Outline each blood parasite and name the species.
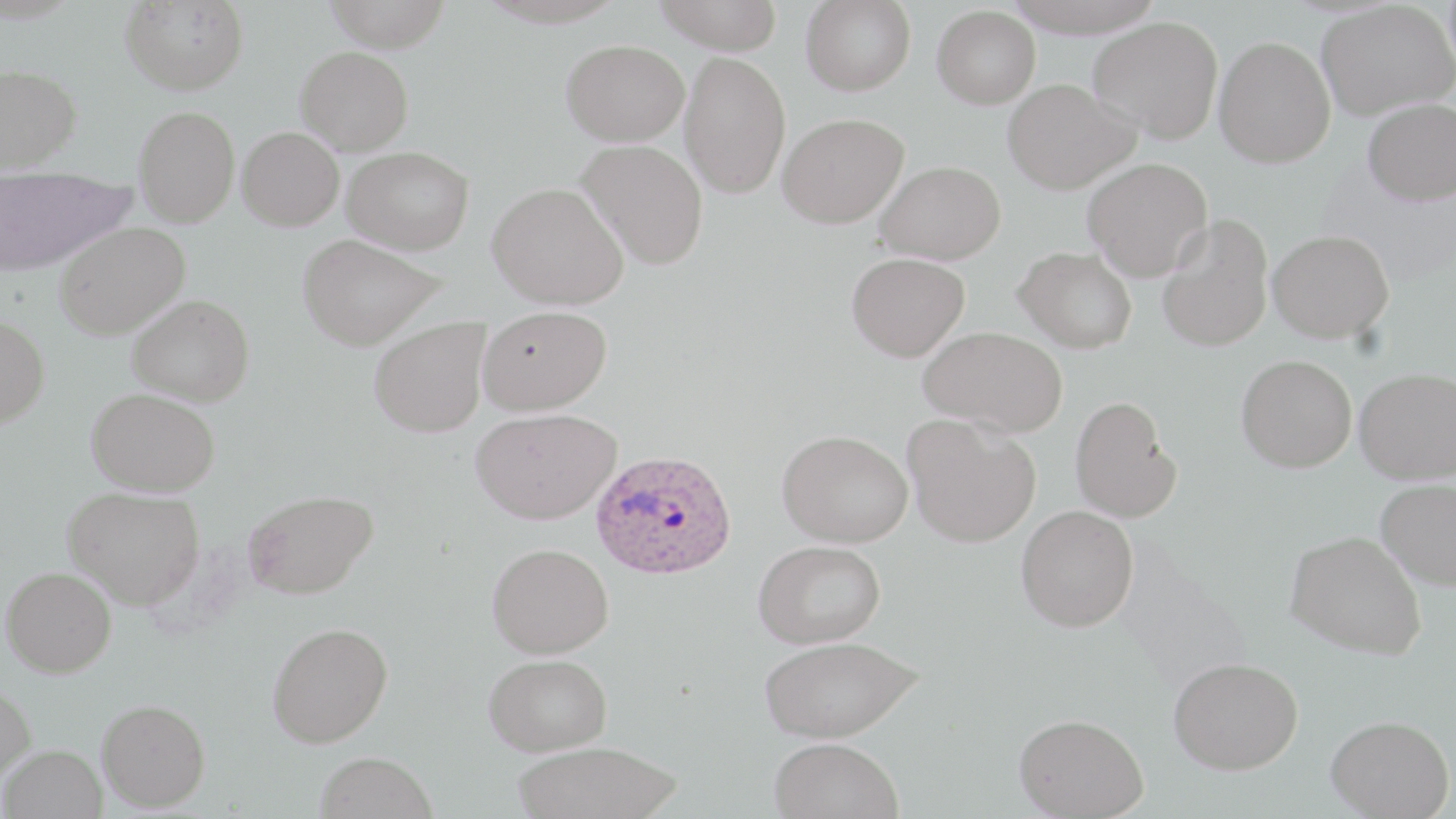

Approximate bounding boxes as named x1/y1/x2/y2 corners in pixels.
Plasmodium ovale-infected red blood cells: (x1=590, y1=448, x2=737, y2=580).
No Plasmodium falciparum, Plasmodium malariae, Plasmodium vivax, Babesia divergens, or Trypanosoma brucei observed.

Uninfected red blood cell locations: (x1=322, y1=0, x2=452, y2=52), (x1=653, y1=0, x2=785, y2=54), (x1=801, y1=0, x2=916, y2=96), (x1=119, y1=1, x2=249, y2=95), (x1=1316, y1=1, x2=1455, y2=120), (x1=932, y1=5, x2=1040, y2=108), (x1=1088, y1=16, x2=1224, y2=143), (x1=1214, y1=36, x2=1336, y2=168), (x1=561, y1=39, x2=690, y2=146), (x1=295, y1=46, x2=414, y2=155), (x1=679, y1=51, x2=791, y2=199), (x1=0, y1=64, x2=82, y2=173), (x1=1002, y1=78, x2=1141, y2=194), (x1=1363, y1=98, x2=1456, y2=206), (x1=134, y1=106, x2=239, y2=227), (x1=777, y1=112, x2=909, y2=228), (x1=237, y1=126, x2=344, y2=230), (x1=577, y1=139, x2=709, y2=269), (x1=342, y1=146, x2=474, y2=255), (x1=1082, y1=157, x2=1213, y2=282), (x1=875, y1=160, x2=1006, y2=264), (x1=0, y1=169, x2=136, y2=276), (x1=487, y1=182, x2=628, y2=309), (x1=1157, y1=215, x2=1274, y2=353), (x1=54, y1=221, x2=190, y2=340), (x1=1267, y1=229, x2=1393, y2=343), (x1=297, y1=233, x2=446, y2=351), (x1=1014, y1=245, x2=1137, y2=353), (x1=846, y1=252, x2=970, y2=362), (x1=127, y1=294, x2=254, y2=406), (x1=477, y1=305, x2=611, y2=414), (x1=0, y1=315, x2=49, y2=428), (x1=369, y1=316, x2=490, y2=437), (x1=918, y1=325, x2=1068, y2=437), (x1=1236, y1=354, x2=1356, y2=472), (x1=1354, y1=367, x2=1456, y2=484), (x1=86, y1=387, x2=220, y2=497), (x1=1070, y1=395, x2=1181, y2=523), (x1=470, y1=407, x2=621, y2=524), (x1=903, y1=414, x2=1041, y2=548), (x1=776, y1=429, x2=913, y2=548), (x1=1375, y1=478, x2=1456, y2=589), (x1=63, y1=487, x2=205, y2=608), (x1=243, y1=489, x2=377, y2=599), (x1=1016, y1=505, x2=1138, y2=632), (x1=1285, y1=530, x2=1426, y2=660), (x1=752, y1=540, x2=886, y2=649), (x1=486, y1=542, x2=613, y2=659), (x1=2, y1=567, x2=116, y2=678), (x1=267, y1=622, x2=393, y2=748), (x1=758, y1=635, x2=922, y2=743), (x1=483, y1=653, x2=612, y2=756), (x1=1167, y1=656, x2=1303, y2=774), (x1=0, y1=684, x2=36, y2=786), (x1=96, y1=699, x2=211, y2=811), (x1=1013, y1=713, x2=1149, y2=818), (x1=1326, y1=715, x2=1454, y2=818), (x1=768, y1=737, x2=904, y2=819), (x1=511, y1=740, x2=684, y2=818), (x1=0, y1=744, x2=106, y2=819), (x1=315, y1=751, x2=437, y2=819). Slide-level diagnosis: Plasmodium ovale. Thin blood film. 1000x magnification. Image is 1456×819 pixels. Light microscopy. One field of a larger specimen. May-Grünwald-Giemsa-stained preparation.